Assess the morphology of the red blood cells.
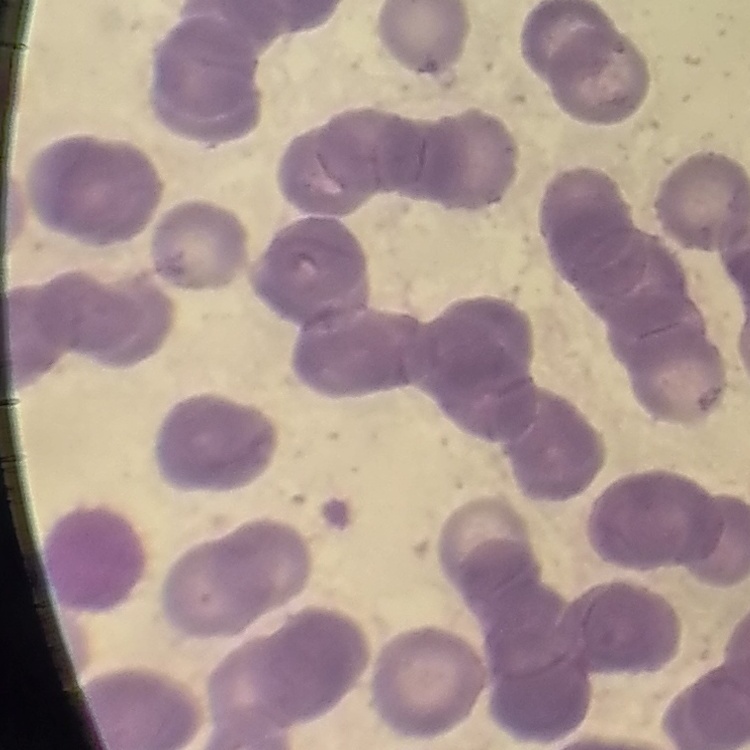
They show rouleaux formation.

One tile cut from a larger photomicrograph. Field's or Giemsa stain. Thin blood smear.